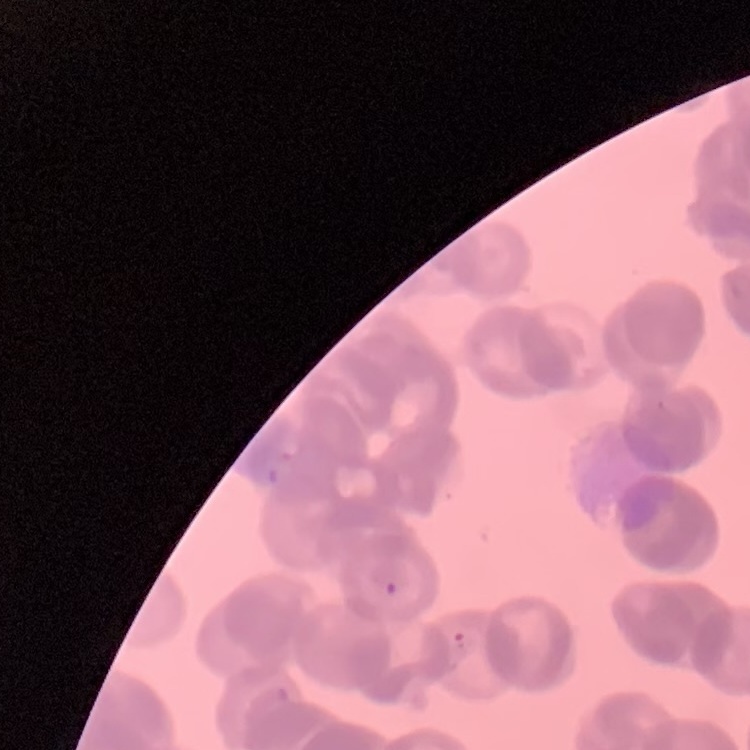
The red blood cells show rouleaux formation. Field's or Giemsa stain. Thin peripheral smear. Square crop of a larger photomicrograph.